Assess this cell for malaria.
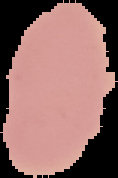
Uninfected.

Summary:
  - Image type: cell region segmented out of the field of view; surrounding area masked to black
  - Image size: 118×178 pixels
  - Preparation: thin blood film